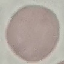 Malaria status: uninfected. Automatically extracted cell patch, resized to 64 × 64 pixels. Thin blood smear. Acquired by smartphone through the microscope eyepiece. Giemsa stain.